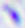

Captured at 400x magnification. Toxoplasma gondii is shown. Photomicrograph.